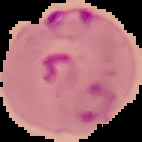
Image is 142×142 pixels. The area outside the segmented cell region is set to black. Malaria status: parasitized. From a thin blood smear.